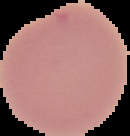
Summary:
  - Image size: 130×136 pixels
  - Image type: segmented cell region on a black background
  - Preparation: thin blood smear
  - Result: no Plasmodium parasites detected